State which parasite is depicted.
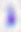

This is Toxoplasma gondii.

Summary:
  - Magnification: 400x
  - Modality: photomicrograph